Assess for Plasmodium parasites.
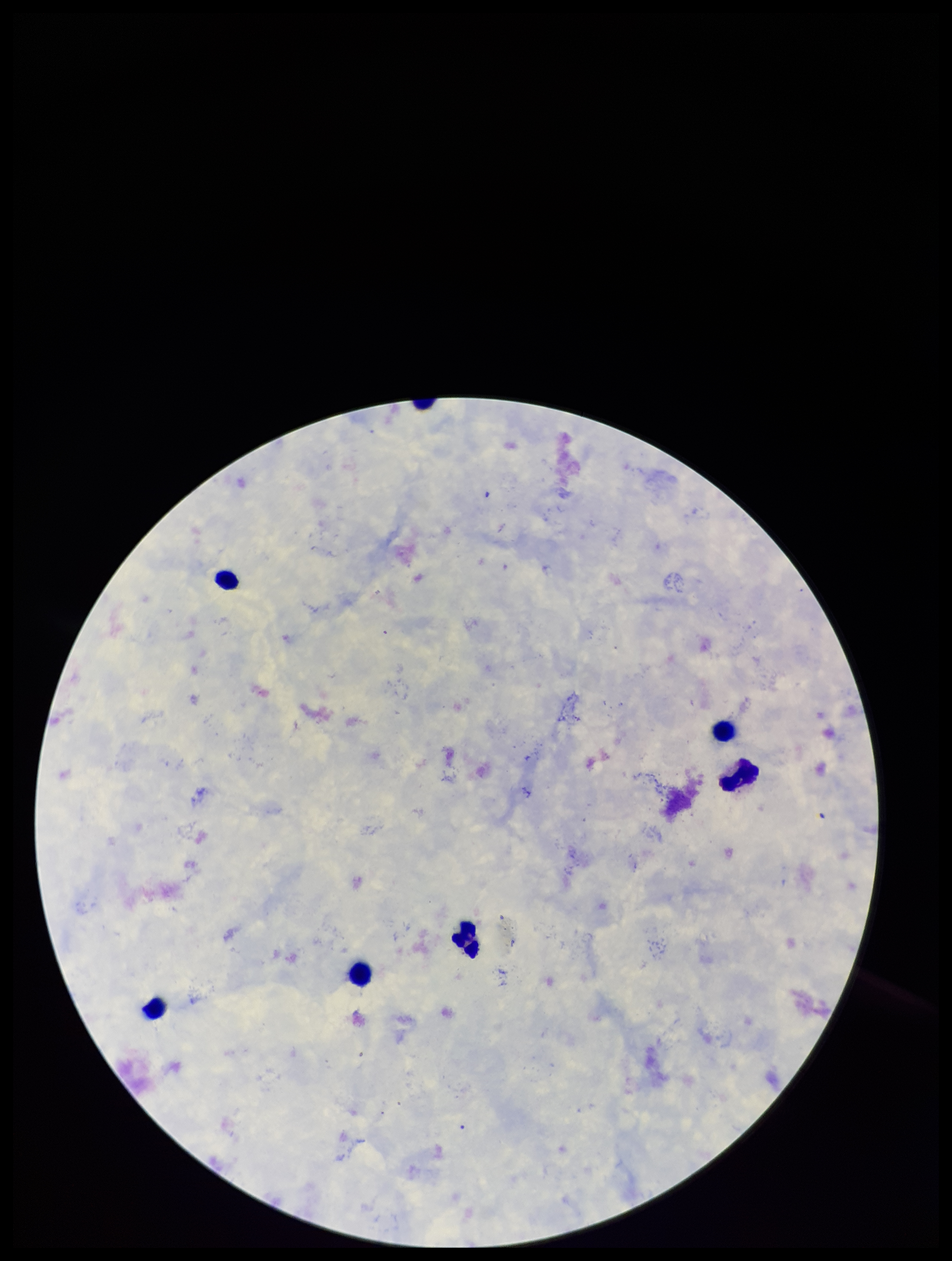
None seen.

leukocyte_count: 7
stain: Giemsa
preparation: thick smear
field_of_view: one from this slide
patient_malaria_status: negative
capture: smartphone photograph through the microscope eyepiece
parasite_count: 0
image_size: 952×1261 pixels